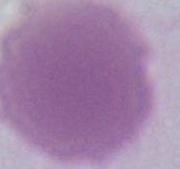
Summary:
  - Modality: photomicrograph
  - Identification: red blood cell
  - Magnification: 1000x